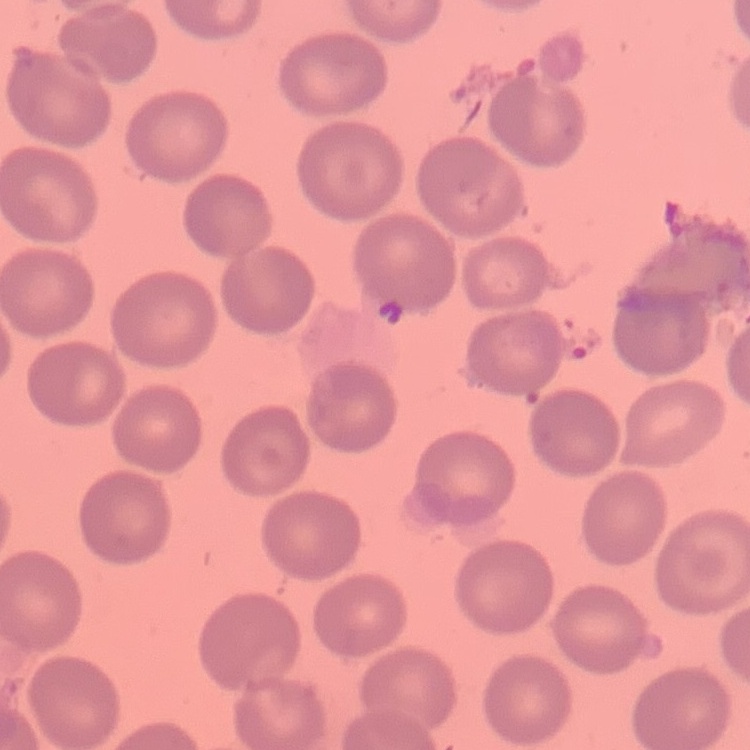

{
  "red_blood_cell_morphology": "no rouleaux formation",
  "stain": "Field's or Giemsa",
  "image_type": "square crop of a larger photomicrograph",
  "preparation": "thin peripheral smear"
}